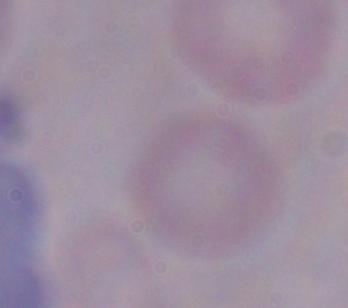

identification = trypanosome
magnification = 1000x
modality = micrograph